Point out each leukocyte.
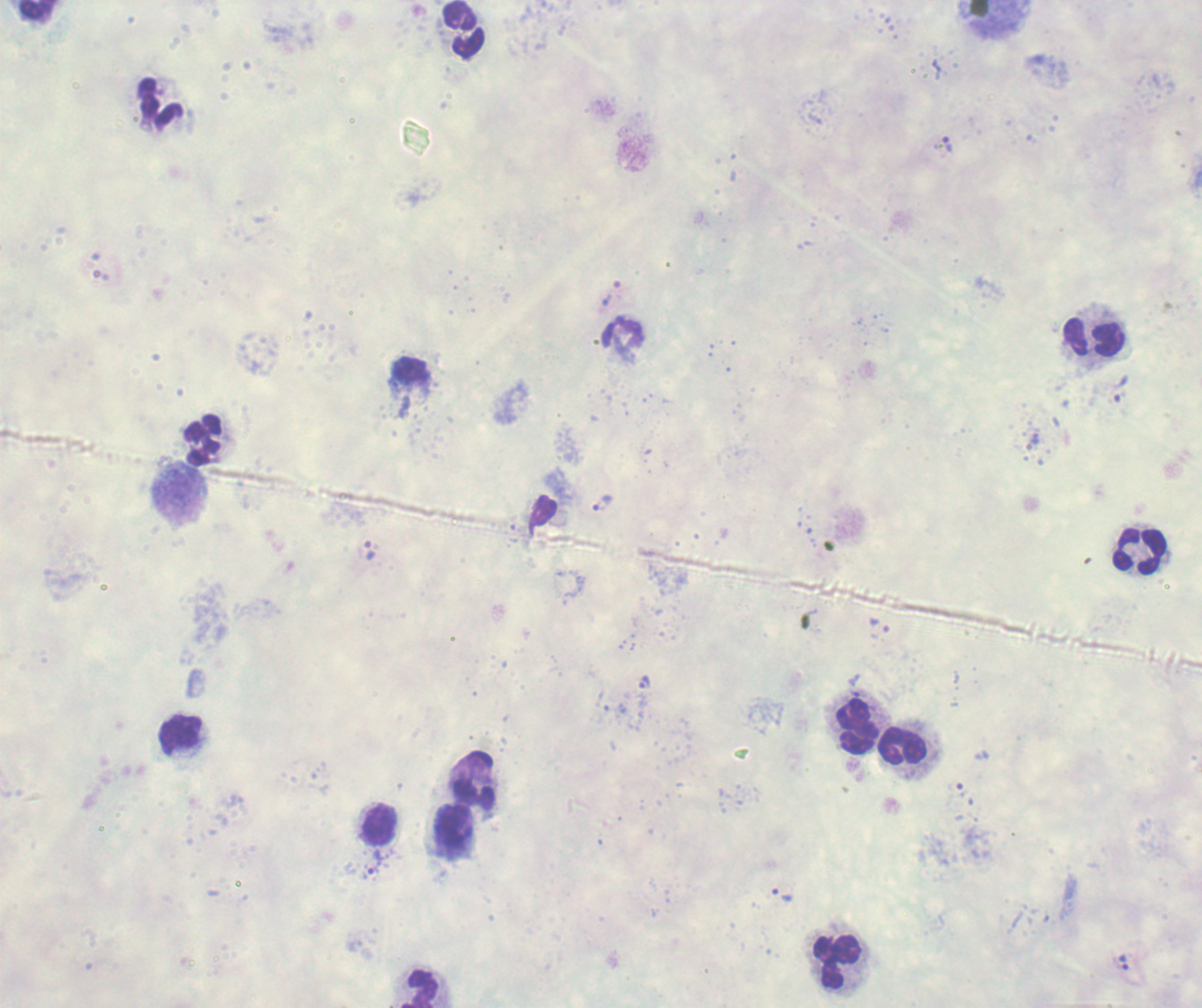

Approximate centers as {x, y} in pixels.
Leukocytes: {37, 11}, {464, 29}, {161, 103}, {622, 333}, {1095, 337}, {411, 369}, {204, 440}, {179, 492}, {1140, 551}, {856, 727}, {180, 736}, {903, 745}, {475, 782}, {379, 825}, {453, 825}, {836, 961}, {420, 988}.

coordinate format = approximate centers as {x, y} in pixels
trophozoite locations = {948, 146}, {610, 294}, {1117, 387}, {1034, 439}, {603, 504}, {368, 550}, {880, 626}, {643, 682}, {854, 692}, {959, 788}, {372, 863}, {781, 896}, {1124, 962}
preparation = thick blood smear
stain = Romanowsky
magnification = 100x
field of view = single
background quality = poor
context = previously used in a real diagnosis
image size = 1202×1008 pixels
result = positive for malaria parasites